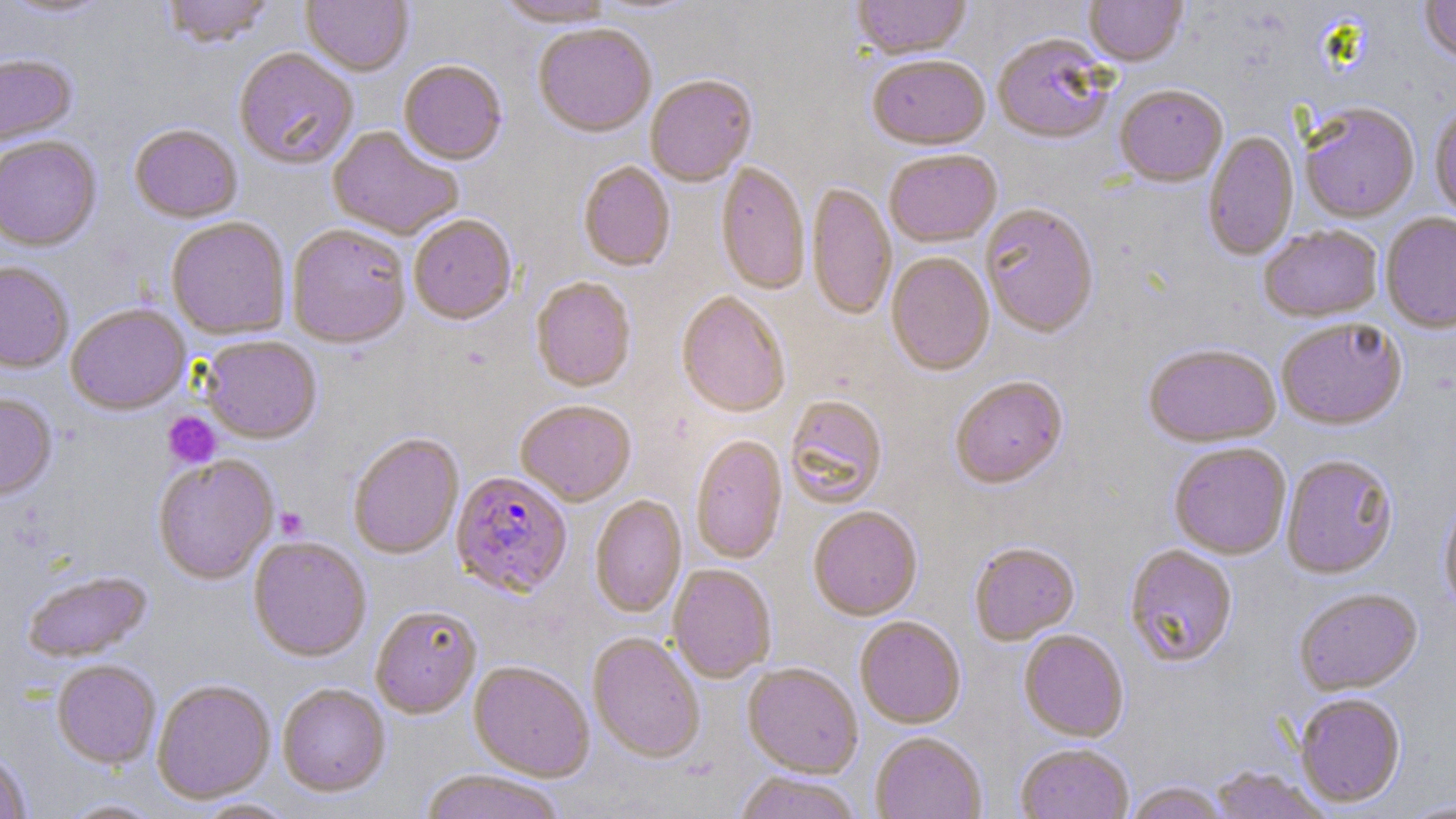
Approximate bounding boxes as (x1,y1)-(x2,y2) corner pairs in pixels. Platelet locations: (163,412)-(221,470), (275,507)-(309,540). Uninfected red blood cell locations: (2,0)-(114,21), (161,0)-(276,49), (301,0)-(413,77), (590,0)-(701,17), (851,0)-(971,61), (1084,0)-(1188,68), (1419,0)-(1456,66), (494,1)-(617,28), (533,25)-(657,139), (992,35)-(1116,146), (233,49)-(359,170), (0,54)-(77,147), (867,57)-(990,152), (398,61)-(507,166), (645,76)-(757,187), (1115,86)-(1228,188), (1300,104)-(1419,222), (1430,105)-(1456,222), (129,125)-(242,223), (327,127)-(464,241), (1203,132)-(1298,260), (0,136)-(102,251), (884,151)-(1002,249), (578,162)-(675,272), (716,164)-(810,295), (807,184)-(896,322), (980,205)-(1099,338), (1380,213)-(1456,334), (408,215)-(517,325), (166,217)-(290,339), (288,224)-(411,348), (1259,225)-(1383,323), (886,253)-(995,377), (0,261)-(74,372), (531,278)-(636,392), (676,292)-(790,418), (66,304)-(190,415), (1276,319)-(1407,431), (200,336)-(322,444), (1143,344)-(1281,448), (950,377)-(1068,489), (0,393)-(57,500), (784,396)-(887,508), (515,400)-(636,506), (348,433)-(464,559), (690,435)-(787,564), (1169,443)-(1291,560), (1281,455)-(1398,580), (152,456)-(279,583), (1439,493)-(1456,617), (590,495)-(687,618), (808,507)-(922,621), (248,536)-(371,662), (969,543)-(1080,645), (1124,545)-(1238,668), (668,565)-(776,683), (22,570)-(152,662), (1294,589)-(1423,696), (371,605)-(482,719), (855,617)-(966,729), (1019,631)-(1129,743), (588,633)-(705,763), (51,660)-(160,768), (469,661)-(594,781), (743,664)-(863,778), (152,679)-(275,804), (277,684)-(390,797), (1295,694)-(1406,809), (871,732)-(986,819), (1016,744)-(1134,818), (1,749)-(32,818), (1208,767)-(1332,818), (419,771)-(566,819), (734,773)-(862,819), (1123,782)-(1228,819), (57,797)-(169,818), (193,798)-(300,819), (1398,799)-(1456,818). Plasmodium falciparum-infected red blood cell locations: (451,470)-(572,597). Slide-level diagnosis: Plasmodium falciparum. May-Grünwald-Giemsa-stained preparation. Thin blood smear. Light microscopy. One field of a larger specimen. Image is 1456×819 pixels. 1000x magnification.